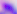

400x magnification. Micrograph. Toxoplasma gondii is shown.